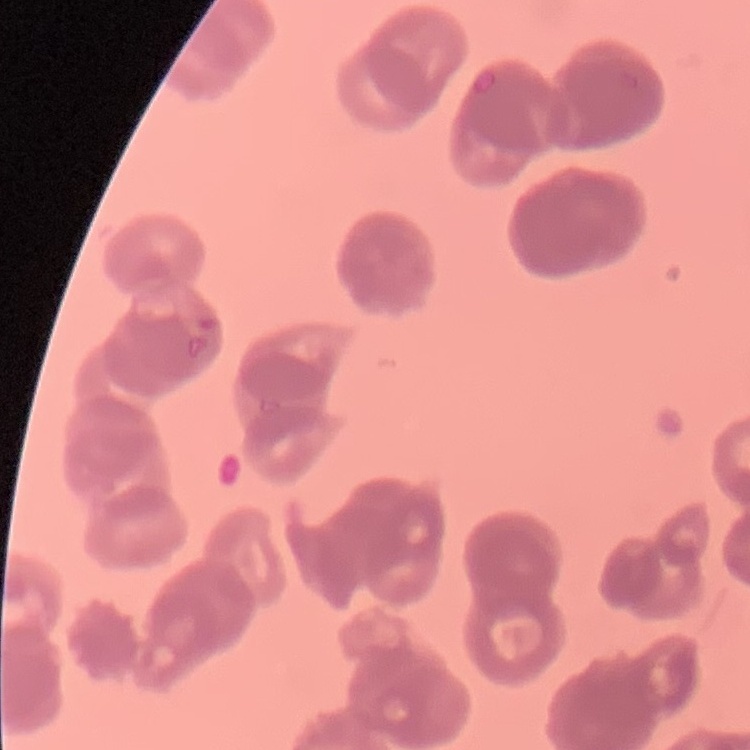 The red blood cells show rouleaux formation. Square crop of a larger photomicrograph. Thin peripheral smear. Stained with either Field's or Giemsa.